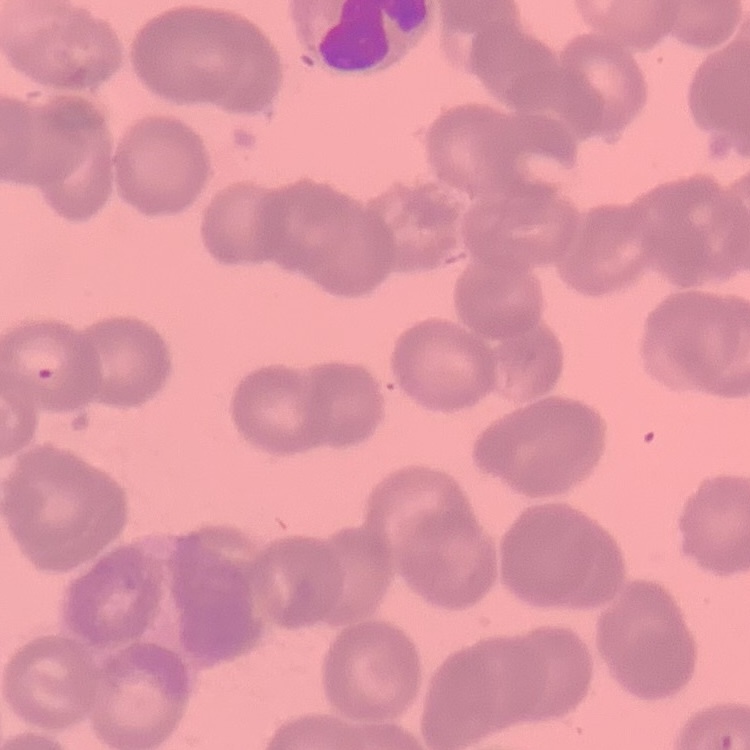
red_blood_cell_morphology: rouleaux formation
stain: Field's or Giemsa
image_type: square crop of a larger photomicrograph
preparation: thin blood film